State which cell type is depicted.
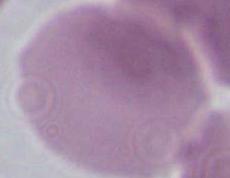
This is an erythrocyte.

magnification = 1000x
modality = micrograph